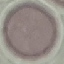
Malaria status: uninfected. Automatically extracted cell patch, resized to 64 × 64 pixels. Photographed with a smartphone camera at the microscope eyepiece. Giemsa-stained preparation. Thin blood smear.